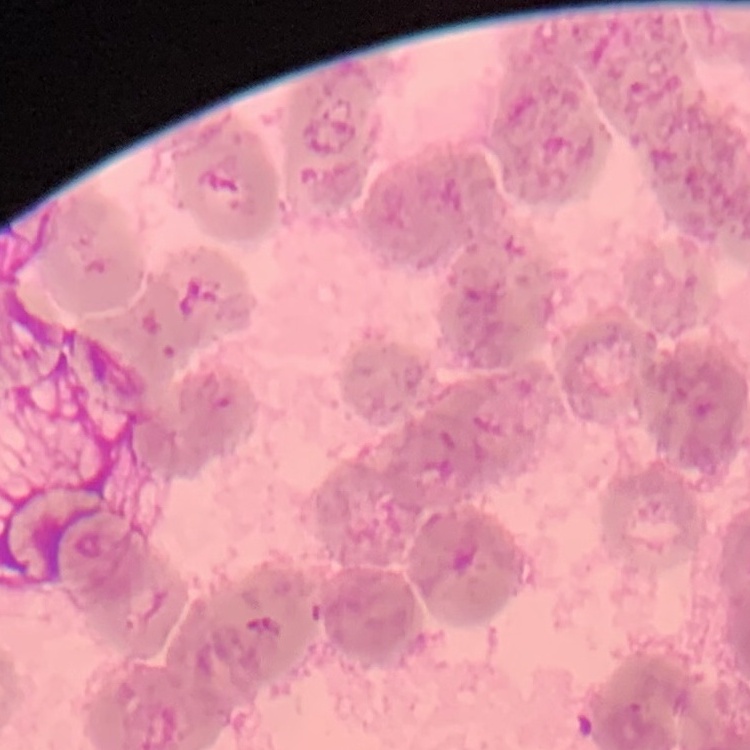
The erythrocytes exhibit rouleaux formation. Field's or Giemsa stain. Thin blood smear. Square crop of a larger photomicrograph.